Give the position of every Plasmodium parasite visible.
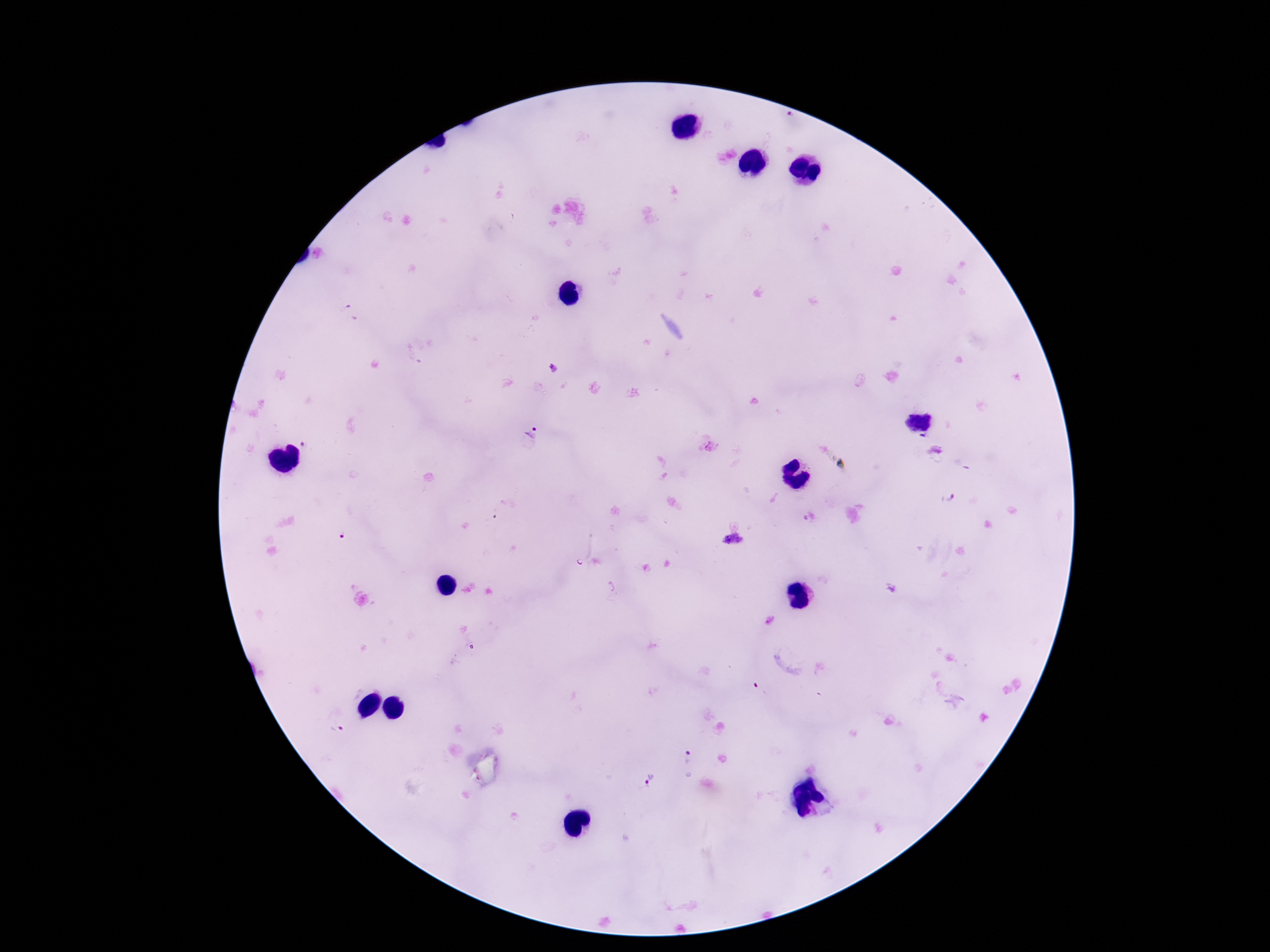
Approximate centers as {x, y} in pixels.
Plasmodium parasites: {920, 422}, {535, 434}, {948, 497}, {733, 541}, {689, 759}, {649, 781}.

image_size: 1270×952 pixels
capture: smartphone camera through the microscope eyepiece
patient_malaria_status: positive
preparation: thick blood film
field_of_view: one from this slide
magnification: 100x
stain: Giemsa